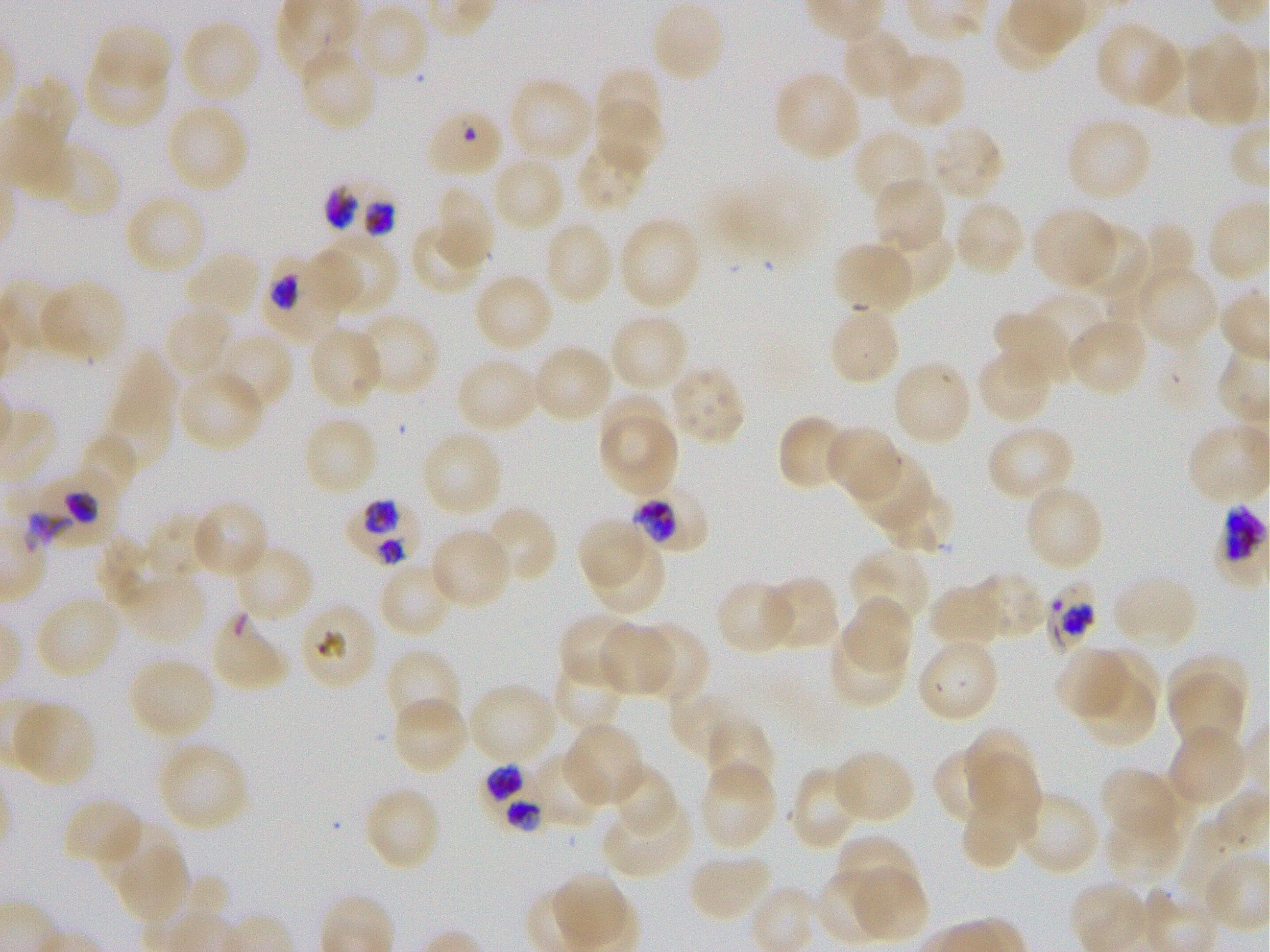
Not every red blood cell is marked. A life-cycle stage — or a range of stages, where the recorded stages span more than one — follows each staged infected red blood cell.
{
  "locations_of_red_blood_cells_of_indeterminate_infection_status": "approximate bounding boxes as {x1, y1, x2, y2} in pixels: {17, 462, 129, 556}, {1031, 572, 1111, 650}, {296, 599, 379, 690}, {210, 605, 292, 689}",
  "stain": "Giemsa",
  "preparation": "thin blood smear",
  "donor_blood_group": "O+",
  "culture": "static in-vitro Plasmodium falciparum strain 3D7",
  "locations_of_infected_red_blood_cells": "approximate bounding boxes as {x1, y1, x2, y2} in pixels: {322, 176, 403, 245}; {265, 254, 354, 341}; {342, 489, 432, 571}; {630, 492, 708, 553} late trophozoite to early schizont; {477, 756, 557, 834}",
  "objective": "100x, oil immersion, numerical aperture 1.25",
  "image_size": "1270×952 pixels",
  "field_of_view": "one from this slide",
  "locations_of_uninfected_red_blood_cells": "approximate bounding boxes as {x1, y1, x2, y2} in pixels: {649, 1, 726, 84}, {354, 4, 430, 82}, {179, 18, 262, 104}, {1095, 21, 1186, 111}, {92, 25, 173, 91}, {841, 27, 917, 102}, {1183, 33, 1263, 129}, {298, 43, 381, 131}, {1148, 44, 1219, 115}, {83, 46, 169, 127}, {883, 50, 966, 130}, {597, 68, 668, 152}, {772, 70, 862, 162}, {507, 76, 595, 166}, {592, 98, 660, 174}, {164, 102, 249, 195}, {423, 107, 506, 179}, {1064, 116, 1153, 204}, {927, 124, 1006, 201}, {852, 128, 931, 208}, {574, 141, 650, 213}, {49, 148, 120, 219}, {491, 154, 566, 234}, {759, 176, 830, 260}, {872, 177, 947, 255}, {702, 182, 773, 266}, {433, 184, 494, 271}, {122, 193, 208, 278}, {952, 199, 1026, 279}, {1030, 206, 1119, 289}, {617, 216, 703, 312}, {542, 220, 615, 307}, {409, 221, 488, 295}, {1067, 221, 1148, 304}, {1135, 224, 1196, 295}, {871, 227, 954, 300}, {309, 235, 399, 317}, {831, 240, 916, 315}, {184, 248, 263, 324}, {1132, 263, 1220, 349}, {472, 272, 554, 355}, {37, 280, 128, 363}, {1024, 291, 1106, 372}, {827, 303, 902, 387}, {163, 305, 237, 381}, {994, 308, 1076, 384}, {351, 312, 440, 397}, {609, 312, 689, 395}, {1066, 317, 1149, 398}, {307, 325, 384, 410}, {213, 331, 293, 415}, {530, 343, 614, 425}, {976, 348, 1056, 425}, {103, 354, 175, 478}, {454, 355, 541, 434}, {891, 358, 973, 447}, {665, 364, 748, 447}, {176, 368, 266, 452}, {600, 395, 673, 467}, {778, 414, 853, 491}, {302, 415, 381, 498}, {598, 417, 680, 497}, {984, 424, 1075, 503}, {824, 426, 904, 502}, {420, 429, 505, 519}, {78, 433, 140, 502}, {851, 451, 936, 540}, {1022, 483, 1106, 572}, {877, 486, 955, 555}, {190, 498, 269, 580}, {481, 506, 558, 586}, {146, 516, 212, 580}, {578, 519, 644, 586}, {429, 526, 513, 611}, {95, 540, 161, 604}, {233, 542, 315, 623}, {590, 543, 665, 614}, {850, 546, 930, 628}, {378, 563, 456, 639}, {110, 566, 217, 651}, {969, 572, 1047, 641}, {1112, 572, 1201, 651}, {761, 576, 841, 651}, {715, 579, 798, 655}, {927, 584, 1007, 649}, {33, 594, 123, 680}, {839, 596, 914, 677}, {558, 613, 640, 689}, {597, 623, 675, 697}, {634, 623, 709, 704}, {828, 630, 907, 707}, {916, 637, 1001, 723}, {1054, 646, 1132, 721}, {389, 647, 461, 720}, {1090, 648, 1160, 723}, {552, 652, 627, 730}, {1168, 652, 1247, 719}, {127, 656, 218, 741}, {1077, 673, 1158, 748}, {1167, 676, 1246, 748}, {467, 682, 559, 764}, {668, 685, 749, 762}, {391, 695, 469, 777}, {9, 699, 98, 787}, {704, 715, 775, 797}, {562, 721, 646, 807}, {960, 724, 1035, 798}, {1167, 727, 1249, 809}, {155, 739, 249, 833}, {533, 743, 617, 829}, {929, 746, 1004, 820}, {830, 747, 916, 825}, {968, 756, 1043, 830}, {698, 761, 778, 851}, {606, 763, 678, 840}, {788, 766, 860, 850}, {1100, 768, 1193, 845}, {362, 785, 441, 872}, {960, 788, 1036, 870}, {1020, 790, 1101, 875}, {62, 797, 145, 869}, {602, 797, 695, 879}, {1104, 810, 1186, 886}, {1173, 816, 1247, 916}, {101, 821, 182, 889}, {832, 835, 920, 909}, {117, 850, 191, 924}, {687, 850, 774, 923}, {844, 865, 928, 942}, {816, 871, 886, 939}"
}